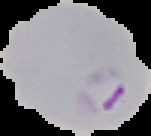
image type = cell region segmented out of the field of view; surrounding area masked to black
image size = 151×136 pixels
preparation = thin blood film
result = malaria parasites detected